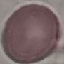
{
  "result": "no malaria parasites detected",
  "preparation": "thin blood film",
  "capture": "smartphone through the microscope eyepiece",
  "stain": "Giemsa",
  "image_type": "automatically extracted cell patch, resized to 64 × 64 pixels"
}